Locate and identify every blood parasite.
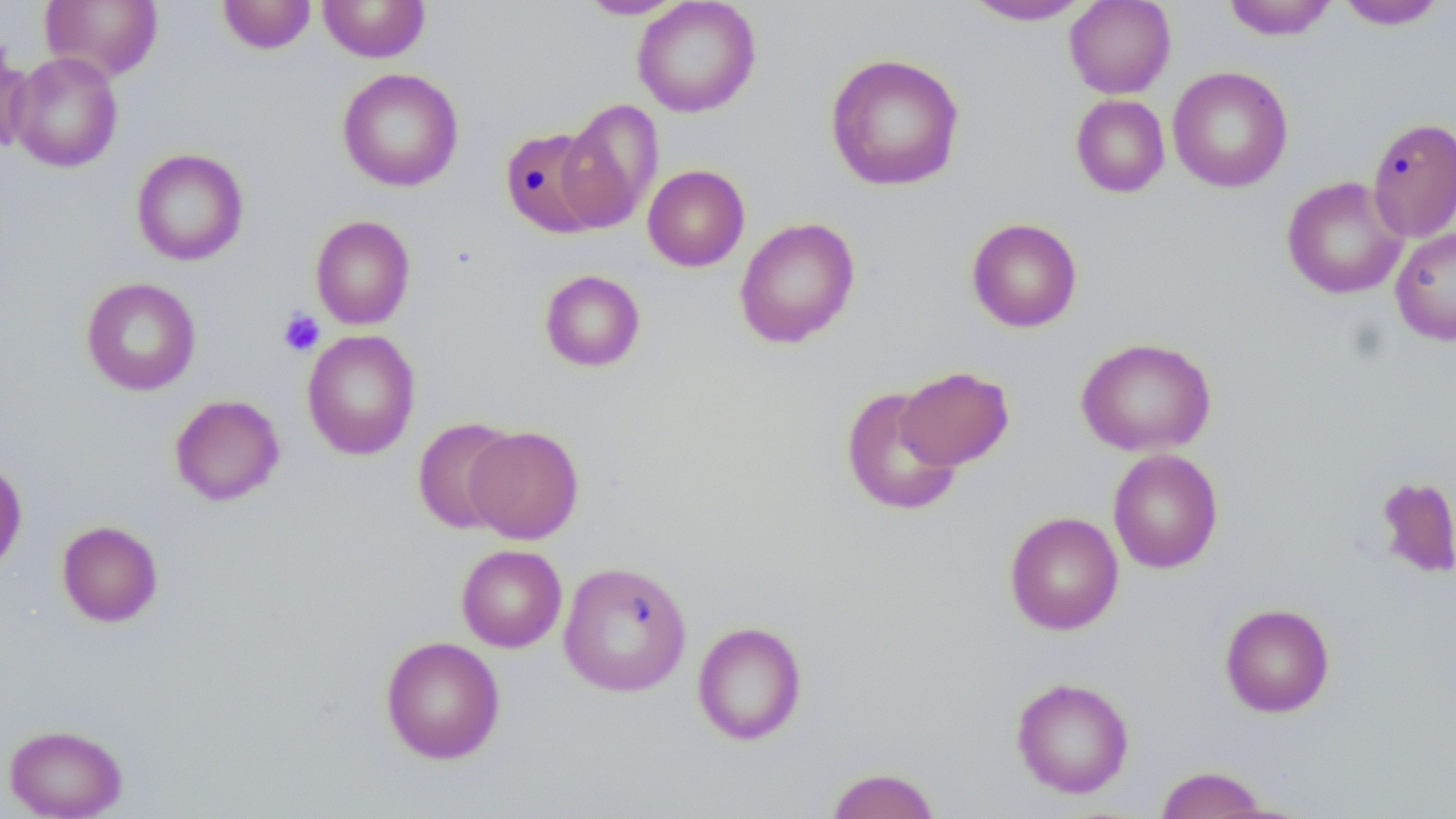
No blood parasites seen.

{
  "slide_level_diagnosis": "no evidence of blood parasites",
  "preparation": "thin blood smear",
  "field_of_view": "one of a larger specimen",
  "stain": "May-Grünwald-Giemsa",
  "image_size": "1456×819 pixels",
  "uninfected_red_blood_cell_locations": "approximate bounding boxes as (x1,y1)-(x2,y2) corner pairs in pixels: (40,0)-(163,82), (217,0)-(316,54), (318,0)-(430,62), (575,0)-(690,20), (632,0)-(761,117), (1064,0)-(1176,98), (1220,0)-(1338,41), (961,1)-(1093,25), (1335,1)-(1449,30), (0,36)-(34,156), (7,51)-(123,172), (824,52)-(966,192), (1167,66)-(1293,193), (337,68)-(464,192), (1070,94)-(1170,198), (556,98)-(664,233), (1367,117)-(1456,243), (500,127)-(609,238), (131,148)-(249,266), (643,164)-(750,271), (1281,176)-(1408,299), (310,215)-(415,329), (734,217)-(860,349), (966,217)-(1083,332), (1390,227)-(1456,345), (539,269)-(646,372), (80,276)-(201,396), (302,329)-(420,460), (1075,337)-(1217,457), (896,366)-(1014,470), (841,386)-(963,517), (169,394)-(285,506), (412,416)-(520,534), (464,425)-(584,544), (1108,448)-(1223,574), (0,458)-(27,575), (1375,475)-(1456,579), (1004,511)-(1124,635), (57,520)-(163,626), (456,545)-(567,652), (558,560)-(692,697), (1220,602)-(1335,717), (692,621)-(808,746), (380,635)-(506,764), (1011,676)-(1134,799), (3,723)-(128,819), (1153,765)-(1272,819), (824,766)-(942,819)",
  "magnification": "1000x",
  "platelet_locations": "approximate bounding boxes as (x1,y1)-(x2,y2) corner pairs in pixels: (278,308)-(325,357)",
  "modality": "light microscopy"
}